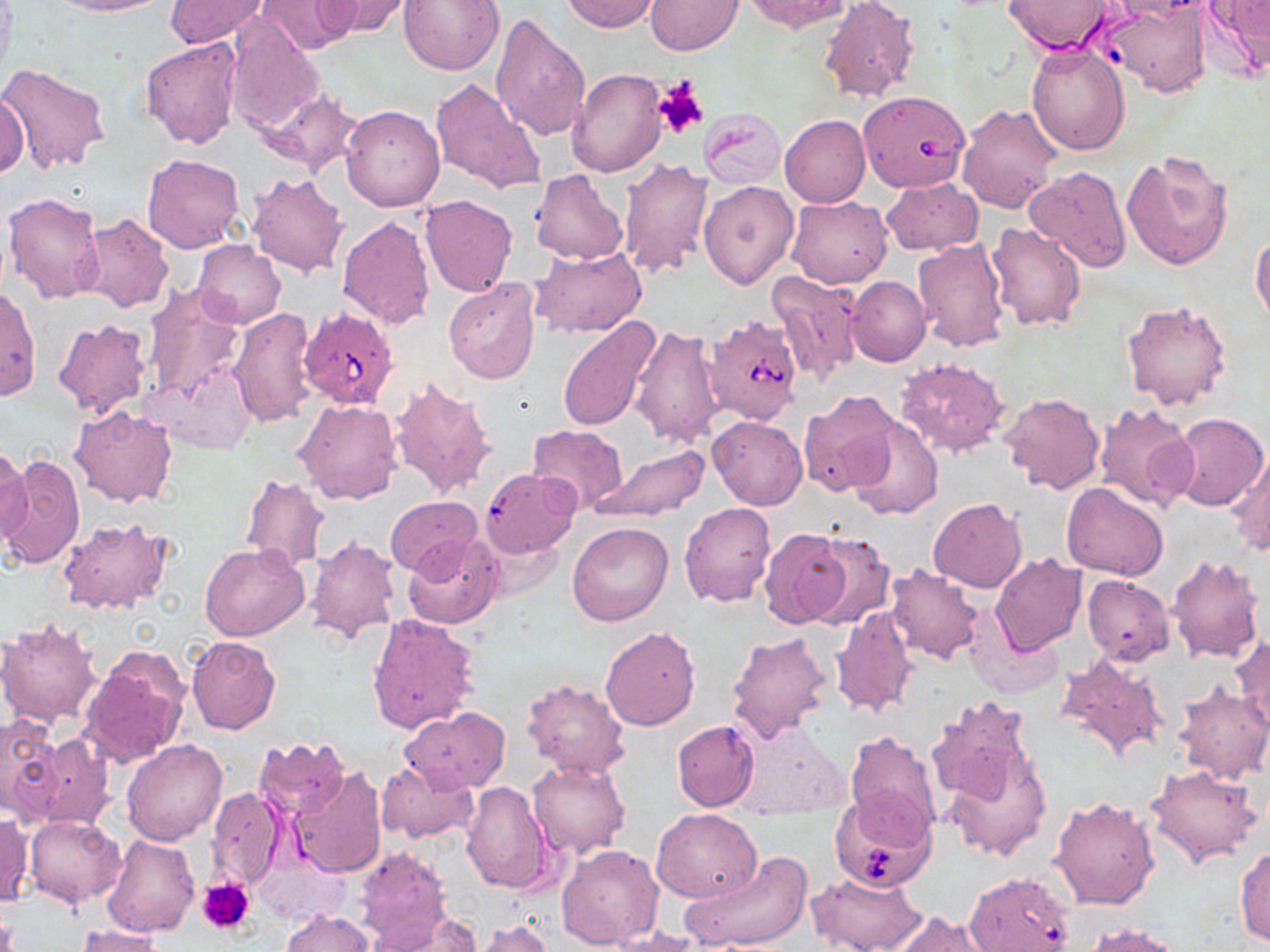
{
  "slide_level_diagnosis": "Babesia divergens",
  "field_of_view": "single",
  "babesia_divergens_infected_red_blood_cell_locations": "approximate bounding boxes as named x1/y1/x2/y2 corners in pixels: (x1=856, y1=89, x2=971, y2=193), (x1=299, y1=307, x2=396, y2=411), (x1=666, y1=312, x2=788, y2=431), (x1=827, y1=786, x2=935, y2=890), (x1=963, y1=871, x2=1075, y2=952)",
  "stain": "May-Grünwald-Giemsa",
  "image_size": "1270×952 pixels",
  "modality": "optical microscopy",
  "preparation": "thin blood film",
  "uninfected_red_blood_cell_locations": "approximate bounding boxes as named x1/y1/x2/y2 corners in pixels: (x1=47, y1=0, x2=166, y2=16), (x1=258, y1=0, x2=360, y2=56), (x1=319, y1=0, x2=415, y2=38), (x1=399, y1=0, x2=504, y2=75), (x1=560, y1=0, x2=660, y2=32), (x1=644, y1=0, x2=742, y2=54), (x1=744, y1=0, x2=850, y2=34), (x1=817, y1=0, x2=920, y2=104), (x1=1004, y1=0, x2=1115, y2=54), (x1=1201, y1=0, x2=1270, y2=79), (x1=164, y1=1, x2=270, y2=49), (x1=1099, y1=3, x2=1211, y2=96), (x1=227, y1=12, x2=324, y2=134), (x1=489, y1=12, x2=592, y2=142), (x1=140, y1=38, x2=242, y2=148), (x1=1026, y1=43, x2=1129, y2=155), (x1=0, y1=63, x2=111, y2=173), (x1=566, y1=70, x2=665, y2=177), (x1=430, y1=76, x2=546, y2=195), (x1=255, y1=88, x2=364, y2=180), (x1=0, y1=91, x2=29, y2=179), (x1=957, y1=103, x2=1064, y2=214), (x1=341, y1=104, x2=444, y2=211), (x1=699, y1=108, x2=785, y2=188), (x1=779, y1=114, x2=870, y2=208), (x1=1122, y1=149, x2=1236, y2=273), (x1=142, y1=153, x2=244, y2=253), (x1=617, y1=155, x2=711, y2=279), (x1=1024, y1=165, x2=1133, y2=273), (x1=530, y1=169, x2=630, y2=265), (x1=245, y1=173, x2=349, y2=279), (x1=880, y1=176, x2=981, y2=255), (x1=699, y1=180, x2=798, y2=289), (x1=4, y1=191, x2=105, y2=304), (x1=420, y1=194, x2=517, y2=296), (x1=786, y1=194, x2=891, y2=288), (x1=77, y1=214, x2=173, y2=314), (x1=337, y1=217, x2=435, y2=330), (x1=985, y1=220, x2=1087, y2=330), (x1=1251, y1=230, x2=1270, y2=327), (x1=913, y1=239, x2=1009, y2=352), (x1=193, y1=241, x2=286, y2=328), (x1=530, y1=246, x2=647, y2=337), (x1=767, y1=271, x2=865, y2=382), (x1=847, y1=274, x2=930, y2=366), (x1=444, y1=278, x2=541, y2=383), (x1=144, y1=284, x2=246, y2=401), (x1=0, y1=286, x2=41, y2=400), (x1=1121, y1=299, x2=1234, y2=412), (x1=228, y1=308, x2=320, y2=428), (x1=558, y1=316, x2=665, y2=432), (x1=53, y1=319, x2=153, y2=419), (x1=630, y1=325, x2=726, y2=449), (x1=895, y1=357, x2=1012, y2=459), (x1=143, y1=362, x2=257, y2=454), (x1=387, y1=374, x2=497, y2=499), (x1=797, y1=389, x2=904, y2=499), (x1=1000, y1=392, x2=1106, y2=494), (x1=293, y1=398, x2=401, y2=505), (x1=1095, y1=401, x2=1197, y2=513), (x1=68, y1=405, x2=178, y2=508), (x1=1169, y1=412, x2=1269, y2=512), (x1=707, y1=416, x2=808, y2=510), (x1=846, y1=418, x2=943, y2=519), (x1=527, y1=424, x2=629, y2=514), (x1=589, y1=444, x2=710, y2=523), (x1=0, y1=446, x2=33, y2=547), (x1=1226, y1=451, x2=1270, y2=556), (x1=0, y1=453, x2=86, y2=570), (x1=241, y1=474, x2=329, y2=573), (x1=1061, y1=483, x2=1170, y2=580), (x1=385, y1=496, x2=482, y2=577), (x1=929, y1=498, x2=1026, y2=592), (x1=680, y1=500, x2=774, y2=605), (x1=59, y1=517, x2=173, y2=614), (x1=567, y1=521, x2=673, y2=625), (x1=757, y1=526, x2=850, y2=629), (x1=803, y1=533, x2=896, y2=630), (x1=403, y1=534, x2=502, y2=629), (x1=306, y1=535, x2=401, y2=644), (x1=200, y1=544, x2=310, y2=641), (x1=990, y1=554, x2=1086, y2=656), (x1=1165, y1=554, x2=1265, y2=664), (x1=885, y1=563, x2=984, y2=665), (x1=1082, y1=574, x2=1173, y2=664), (x1=830, y1=604, x2=917, y2=719), (x1=367, y1=614, x2=479, y2=735), (x1=0, y1=619, x2=103, y2=726), (x1=967, y1=624, x2=1062, y2=699), (x1=598, y1=626, x2=701, y2=731), (x1=725, y1=631, x2=832, y2=745), (x1=185, y1=636, x2=281, y2=734), (x1=1231, y1=636, x2=1270, y2=735), (x1=81, y1=648, x2=190, y2=767), (x1=1053, y1=652, x2=1168, y2=763), (x1=522, y1=678, x2=631, y2=778), (x1=1175, y1=681, x2=1270, y2=782), (x1=926, y1=695, x2=1037, y2=807), (x1=401, y1=707, x2=510, y2=791), (x1=0, y1=714, x2=64, y2=821), (x1=672, y1=720, x2=759, y2=811), (x1=844, y1=730, x2=939, y2=833), (x1=28, y1=732, x2=114, y2=831), (x1=254, y1=736, x2=351, y2=820), (x1=121, y1=738, x2=227, y2=845), (x1=941, y1=748, x2=1051, y2=862), (x1=528, y1=759, x2=629, y2=857), (x1=376, y1=761, x2=479, y2=844), (x1=1145, y1=763, x2=1263, y2=869), (x1=289, y1=766, x2=387, y2=878), (x1=460, y1=781, x2=555, y2=894), (x1=208, y1=786, x2=285, y2=892), (x1=1051, y1=795, x2=1159, y2=909), (x1=651, y1=807, x2=762, y2=903), (x1=0, y1=811, x2=32, y2=907), (x1=23, y1=814, x2=126, y2=907), (x1=102, y1=834, x2=200, y2=936), (x1=353, y1=845, x2=455, y2=951), (x1=557, y1=845, x2=664, y2=950), (x1=1234, y1=846, x2=1270, y2=946), (x1=681, y1=851, x2=813, y2=951), (x1=807, y1=871, x2=925, y2=952), (x1=281, y1=908, x2=375, y2=952), (x1=374, y1=911, x2=481, y2=952), (x1=889, y1=911, x2=996, y2=952), (x1=474, y1=919, x2=552, y2=952), (x1=1084, y1=922, x2=1189, y2=952), (x1=75, y1=925, x2=167, y2=952), (x1=607, y1=927, x2=701, y2=952)",
  "magnification": "1000x",
  "platelet_locations": "approximate bounding boxes as named x1/y1/x2/y2 corners in pixels: (x1=653, y1=78, x2=707, y2=139), (x1=199, y1=877, x2=256, y2=936)"
}